Identify the preparation type.
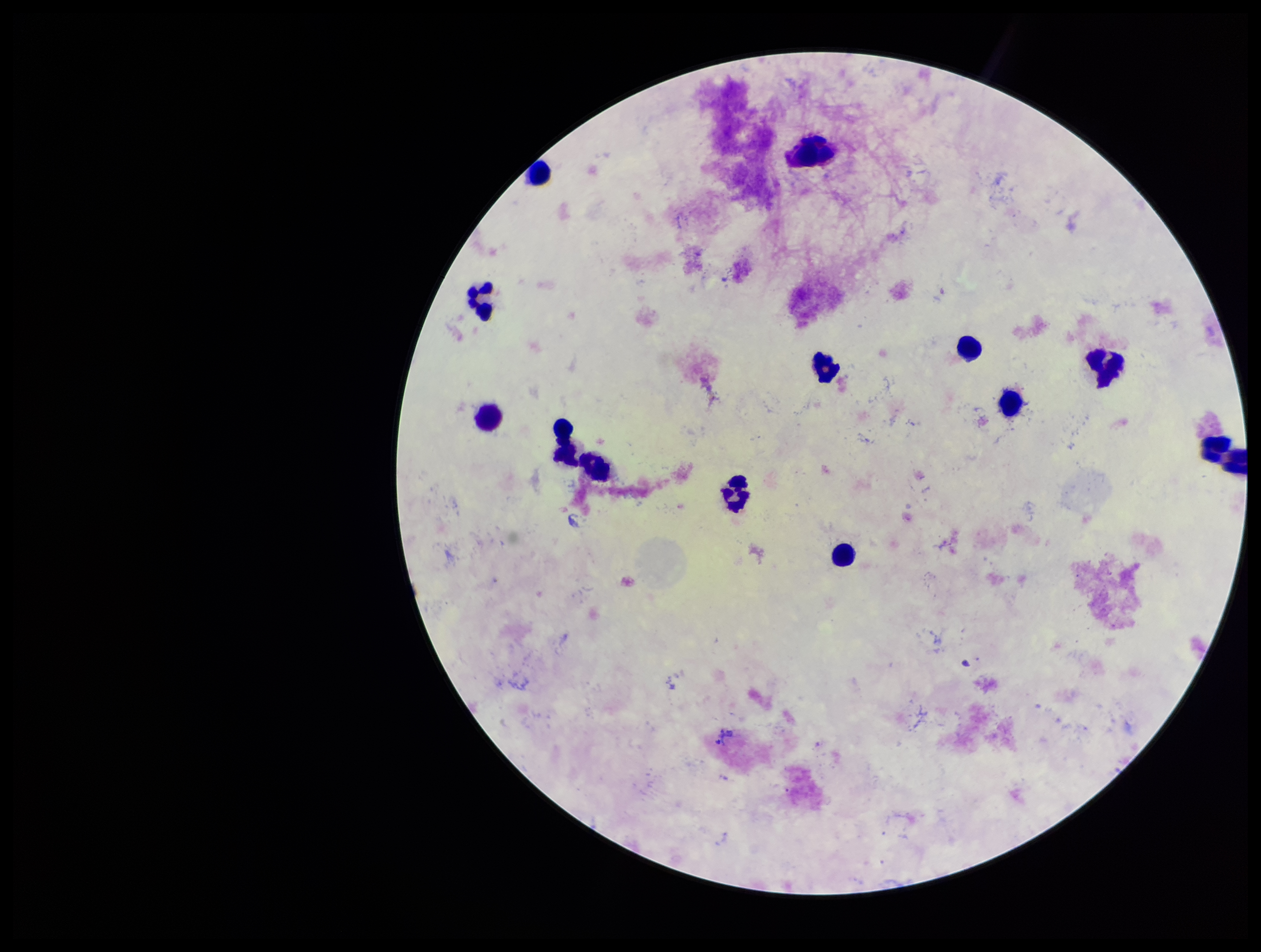
It is a thick blood smear.

Summary:
  - Leukocyte count: 13
  - Species reported for this patient: Plasmodium vivax
  - Capture: smartphone photograph through the microscope eyepiece
  - Stain: Giemsa
  - Field of view: single
  - Parasite count: 0
  - Plasmodium parasites: none seen
  - Patient malaria status: positive
  - Image size: 1261×952 pixels